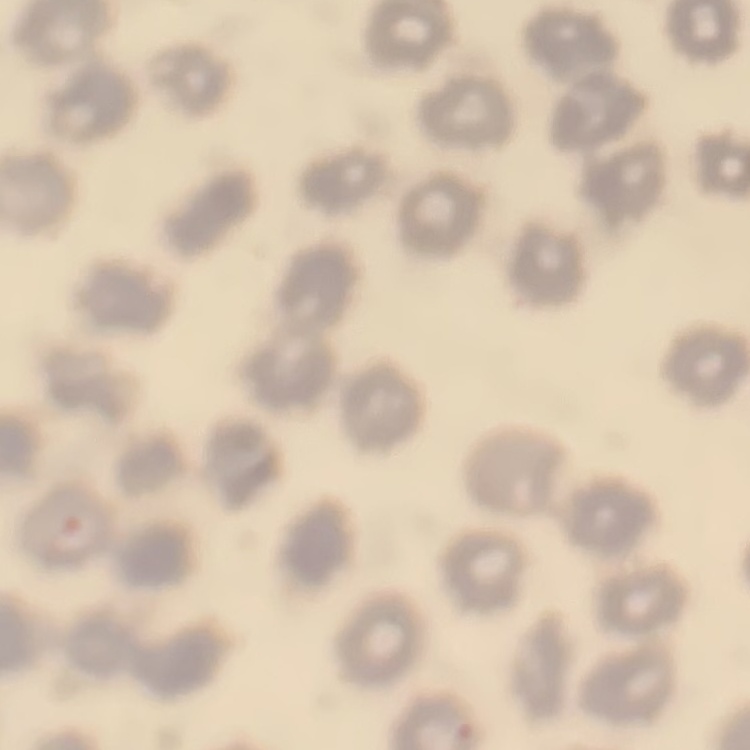
The red blood cells exhibit no rouleaux formation. Thin blood film. Stained with either Field's or Giemsa. One tile cut from a larger photomicrograph.